Classify this cell by malaria status.
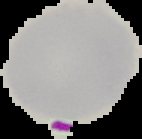

It is parasitized.

From a thin blood smear. Image is 142×139 pixels. The area outside the segmented cell region is set to black.